Report the malaria status of this cell.
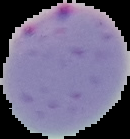
It is parasitized.

Image is 130×139 pixels. From a thin blood film. Cell region segmented out of the field of view; the surrounding area is masked to black.